State which parasite is depicted.
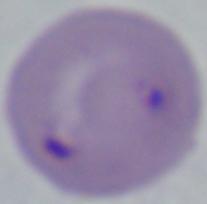
This is Babesia.

Photomicrograph. Captured at 1000x magnification.